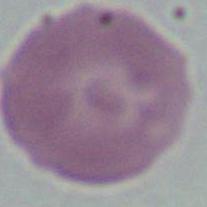 An erythrocyte is seen. 1000x magnification. Micrograph.